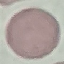

Malaria status: uninfected. Giemsa-stained preparation. Photographed with a smartphone camera at the microscope eyepiece. Automatically extracted cell patch, resized to 64 × 64 pixels. Thin smear of blood.